Name the parasite shown.
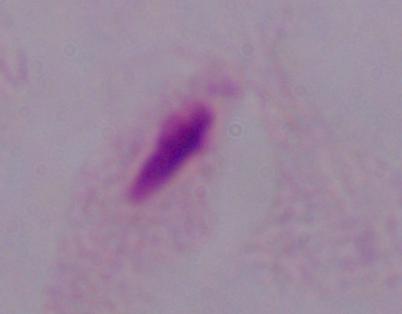

This is a trichomonad.

Photomicrograph. 1000x magnification.